Locate every Trypanosoma brucei.
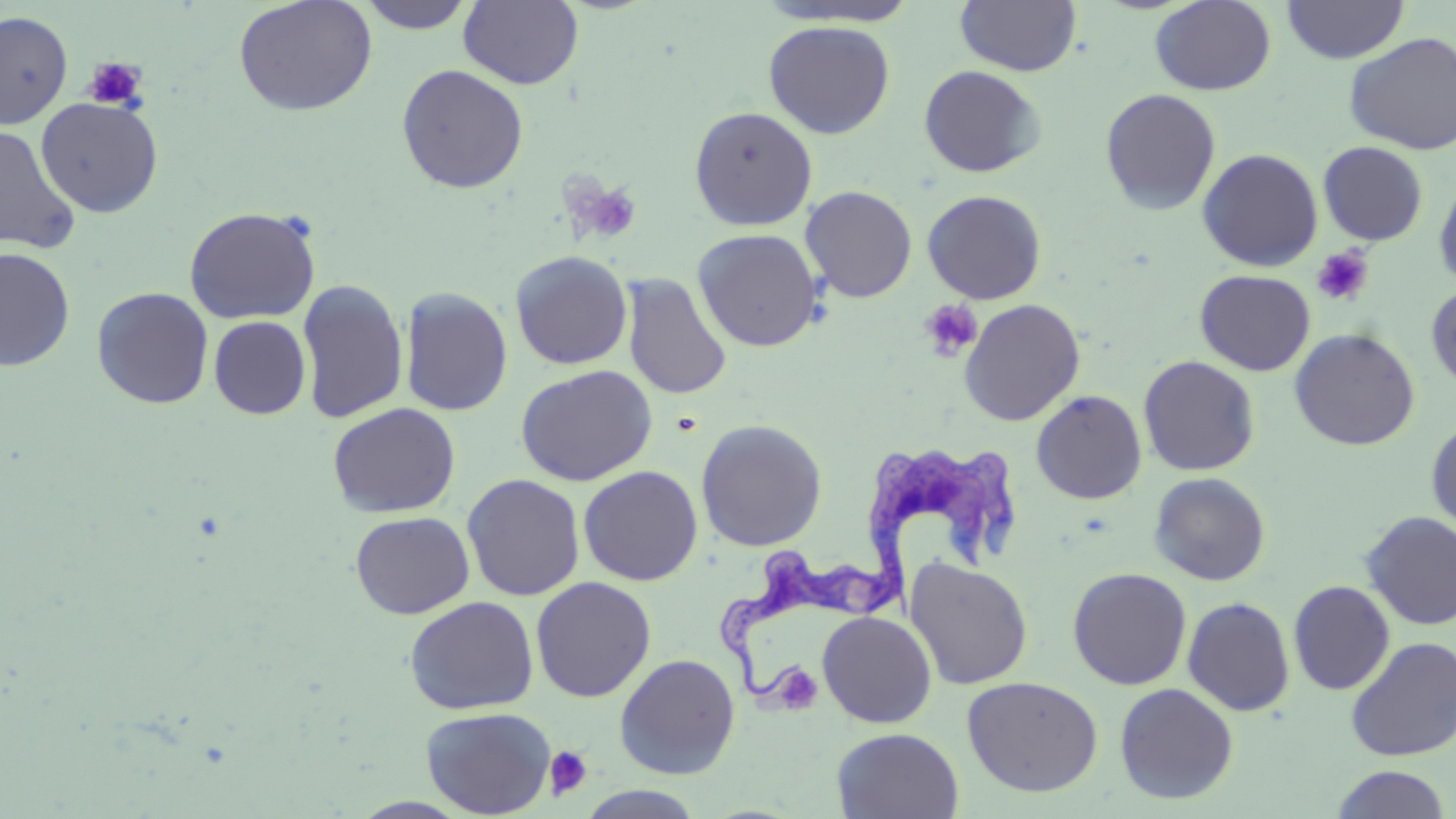
Approximate bounding boxes as (x1,y1)-(x2,y2) corner pairs in pixels.
Trypanosoma brucei: (868,437)-(1032,603), (713,546)-(909,699).

slide-level diagnosis = Trypanosoma brucei
platelet locations = approximate bounding boxes as (x1,y1)-(x2,y2) corner pairs in pixels: (82,55)-(148,111), (574,182)-(641,244), (1310,247)-(1374,306), (919,299)-(983,362), (778,669)-(822,714), (545,746)-(593,800)
uninfected red blood cell locations = approximate bounding boxes as (x1,y1)-(x2,y2) corner pairs in pixels: (233,0)-(379,116), (354,0)-(479,34), (955,0)-(1082,76), (1283,0)-(1408,63), (458,1)-(583,89), (1149,1)-(1276,95), (0,10)-(74,130), (763,20)-(895,139), (1344,32)-(1456,155), (396,64)-(529,194), (919,65)-(1046,177), (1100,88)-(1221,215), (35,96)-(164,217), (689,106)-(817,231), (1,124)-(81,254), (1318,141)-(1428,246), (1197,148)-(1323,272), (1434,173)-(1456,292), (800,186)-(917,303), (921,190)-(1047,304), (184,206)-(322,324), (692,228)-(824,352), (0,246)-(75,371), (509,250)-(633,370), (1195,269)-(1315,376), (621,273)-(733,400), (297,279)-(408,424), (1426,283)-(1456,392), (399,286)-(513,417), (92,287)-(214,409), (959,298)-(1086,426), (209,316)-(311,419), (1289,328)-(1420,451), (1138,355)-(1260,476), (515,364)-(657,486), (1031,389)-(1147,504), (327,402)-(461,518), (1426,418)-(1456,534), (695,419)-(828,551), (578,465)-(703,586), (1148,472)-(1271,586), (462,473)-(585,601), (350,511)-(474,619), (1359,511)-(1456,631), (904,557)-(1034,690), (1068,566)-(1191,690), (530,576)-(657,702), (1288,580)-(1395,696), (403,595)-(540,715), (1182,596)-(1296,716), (817,610)-(937,728), (1346,636)-(1456,762), (614,653)-(741,779), (962,675)-(1104,797), (1115,682)-(1239,804), (420,706)-(555,818), (832,727)-(963,819), (1328,765)-(1453,819), (575,786)-(707,818)
field of view = single
modality = light microscopy
magnification = 1000x
stain = May-Grünwald-Giemsa
preparation = thin blood film
image size = 1456×819 pixels